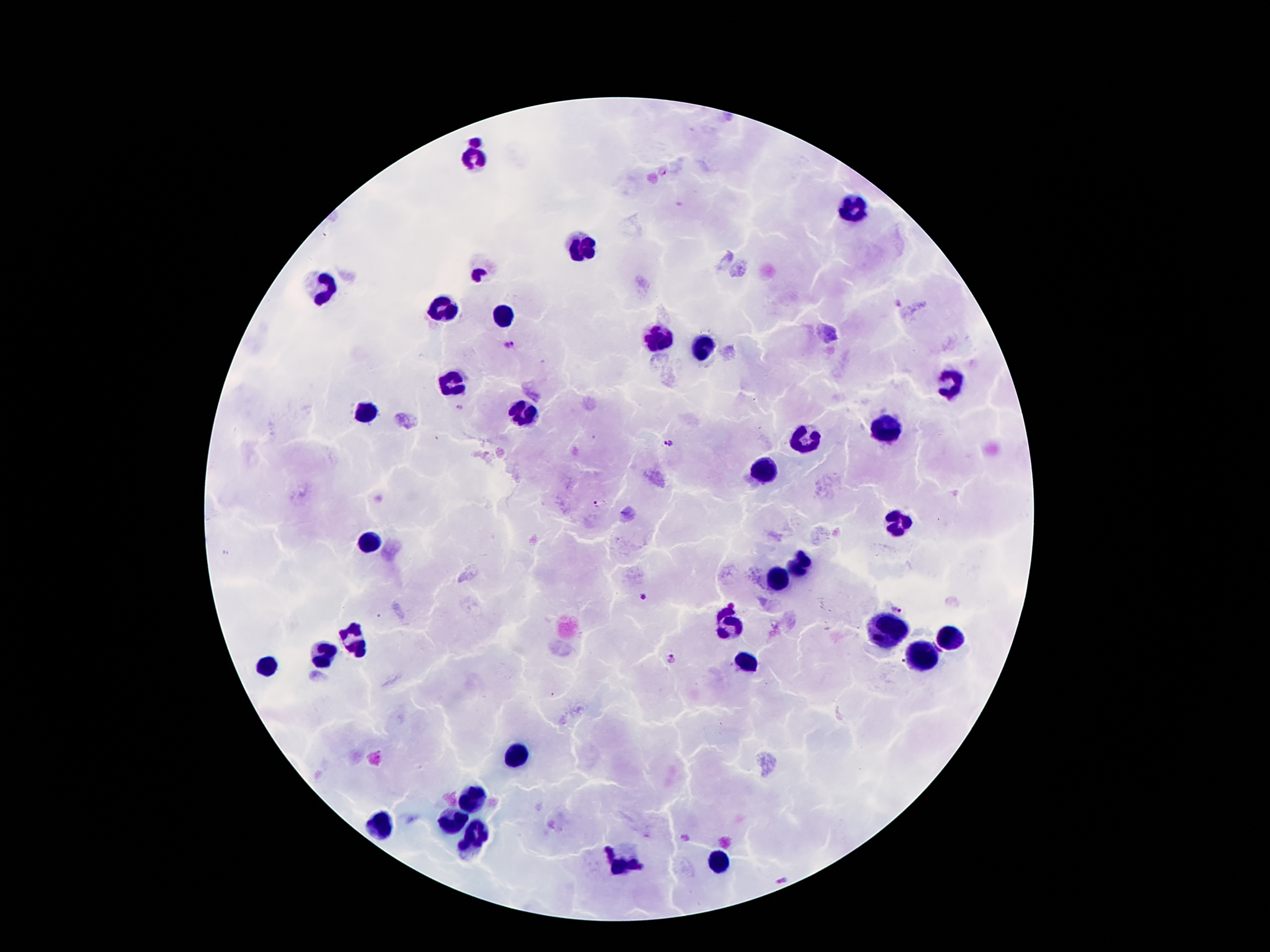

stain: Giemsa
field_of_view: one from this slide
capture: smartphone through the microscope eyepiece
image_size: 1270×952 pixels
malaria_parasite_locations: 'approximate centers as {x, y} in pixels: {662, 169}, {899, 303}, {508, 344}, {459, 406}, {669, 442}, {601, 503}, {643, 598}, {898, 608}, {672, 657}, {687, 837}, {783, 879}'
leukocyte_locations: 'approximate centers as {x, y} in pixels: {473, 154}, {852, 206}, {584, 245}, {320, 290}, {442, 308}, {500, 316}, {655, 338}, {703, 348}, {949, 381}, {453, 383}, {367, 413}, {516, 413}, {886, 426}, {806, 437}, {767, 469}, {893, 525}, {369, 543}, {796, 564}, {776, 579}, {725, 622}, {890, 627}, {949, 639}, {356, 641}, {326, 652}, {925, 657}, {748, 663}, {270, 665}, {520, 751}, {472, 797}, {453, 820}, {380, 827}, {475, 838}, {720, 859}, {623, 864}'
preparation: thick blood film
magnification: 100x
patient_malaria_status: positive for Plasmodium falciparum